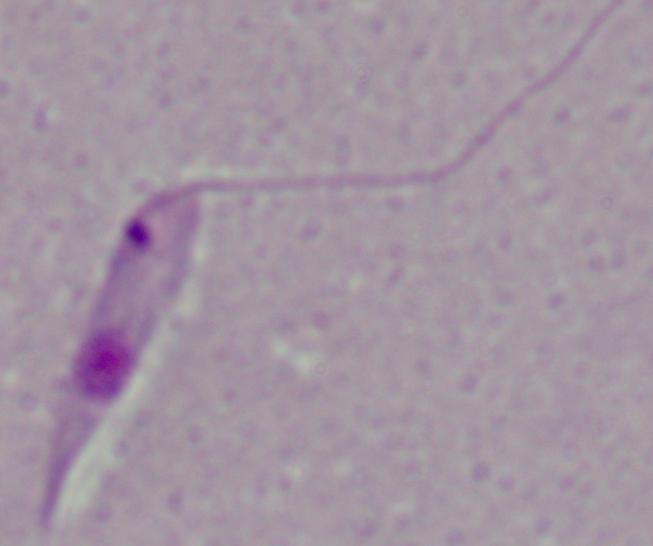 1000x magnification. Photomicrograph. A Leishmania parasite is seen.